Identify the parasite.
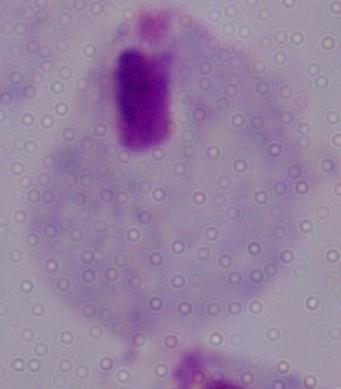
A trichomonad.

Summary:
  - Magnification: 1000x
  - Modality: photomicrograph